State which parasite is depicted.
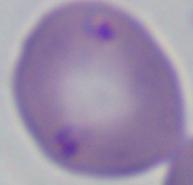

Babesia.

1000x magnification. Micrograph.